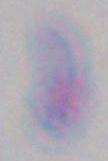
Summary:
  - Magnification: 1000x
  - Identification: Toxoplasma gondii
  - Modality: photomicrograph